Assess for parasitized red blood cells.
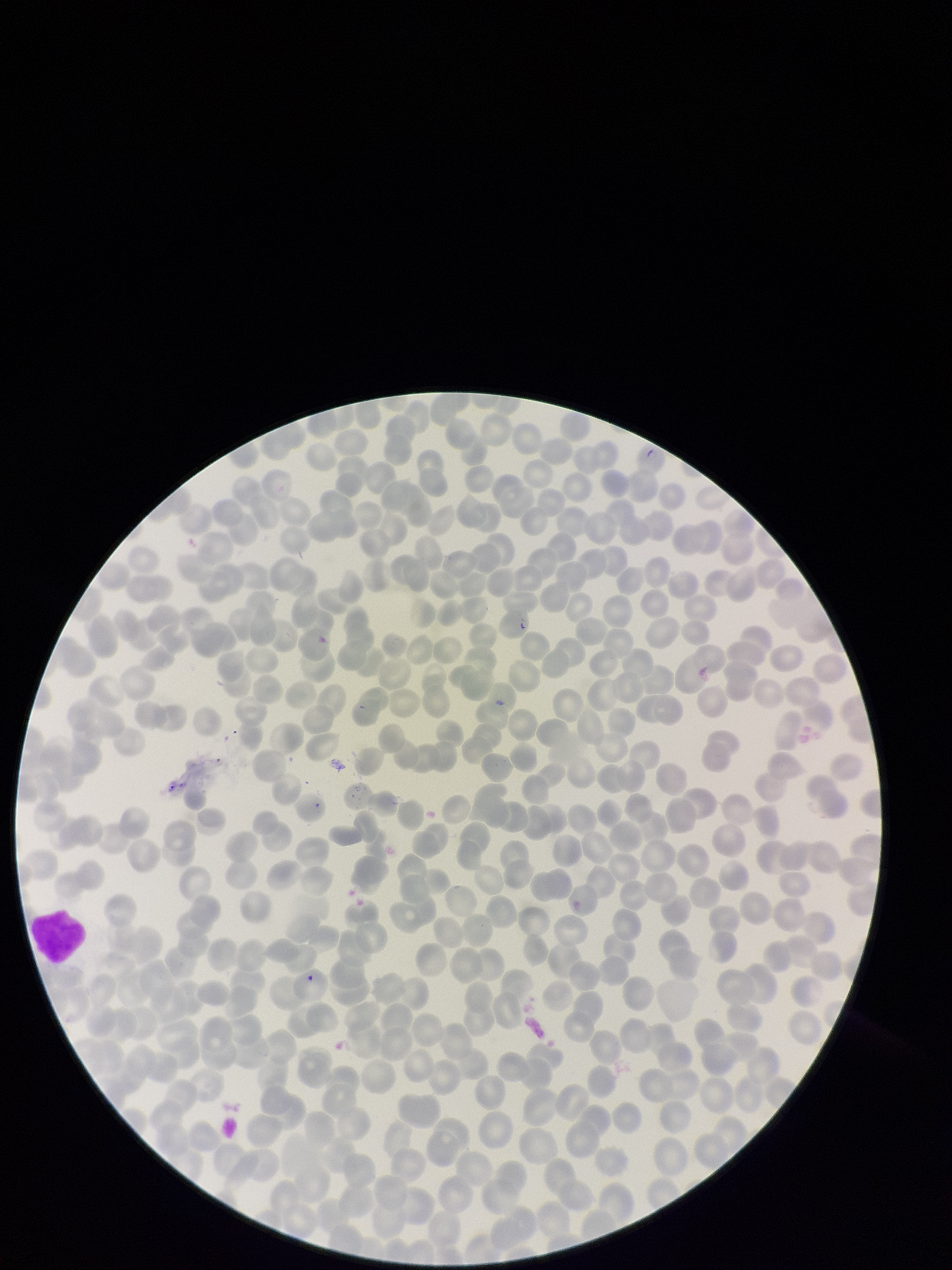
Identified.

Summary:
  - Stain: Giemsa
  - Red blood cell count: 231
  - Field of view: one from this slide
  - Image size: 952×1270 pixels
  - Patient malaria status: positive
  - Capture: smartphone photograph through the microscope eyepiece
  - Preparation: thin
  - Parasitized red blood cell count: 1
  - Species reported for this patient: Plasmodium falciparum